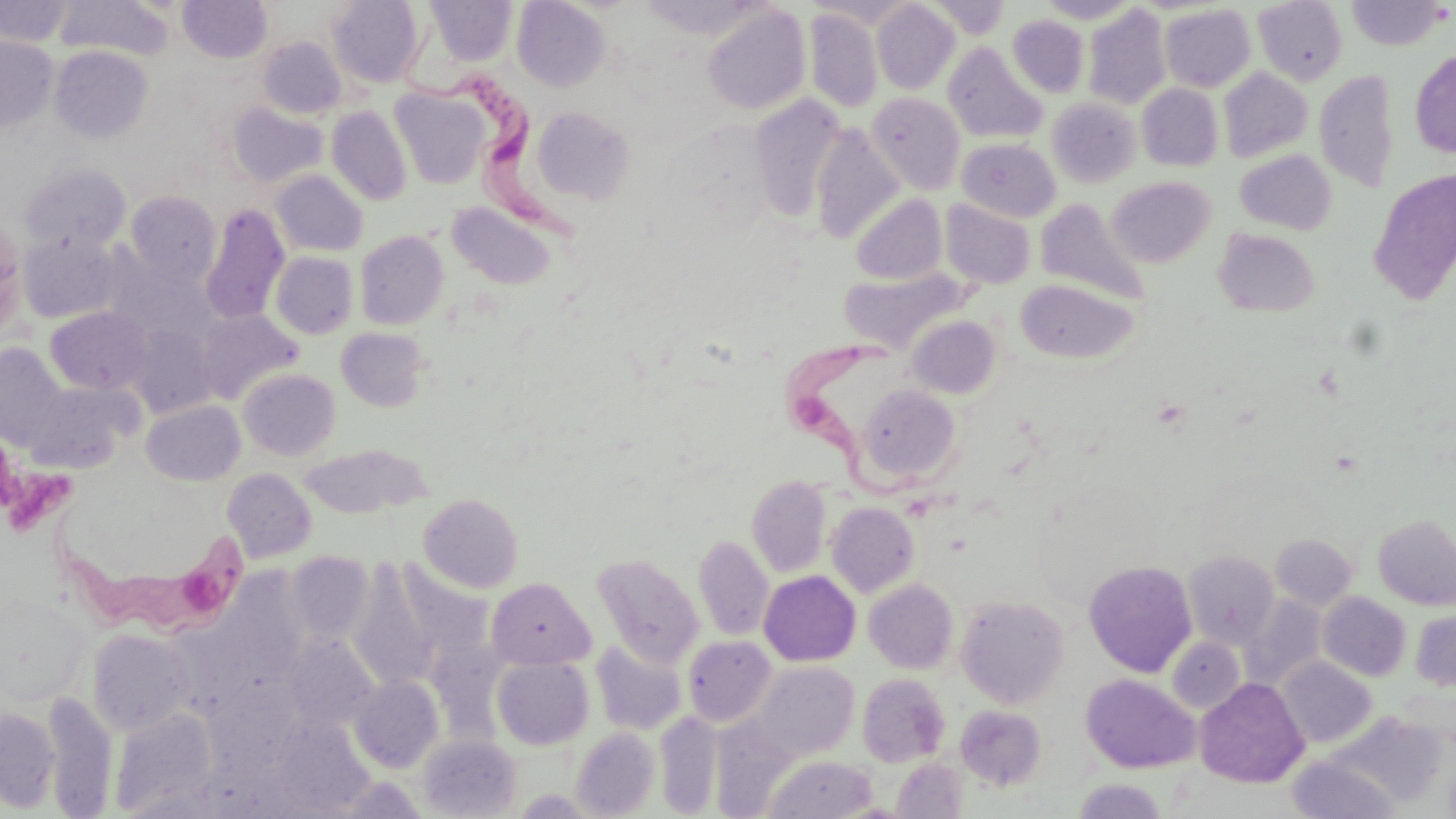
Summary:
  - Coordinate format: approximate bounding boxes as (x1,y1)-(x2,y2) corner pairs in pixels
  - Platelet locations: (11,475)-(72,536)
  - Uninfected red blood cell locations: (54,0)-(174,61), (327,0)-(425,88), (1036,0)-(1141,24), (1254,0)-(1348,85), (0,1)-(72,46), (178,1)-(272,62), (425,1)-(518,66), (512,1)-(610,91), (807,1)-(918,28), (925,1)-(1010,39), (1346,1)-(1449,50), (872,2)-(960,94), (1159,4)-(1256,92), (702,6)-(811,115), (1082,6)-(1171,109), (804,8)-(883,112), (1007,15)-(1090,97), (0,35)-(59,132), (258,36)-(346,119), (942,42)-(1047,144), (50,46)-(153,143), (1410,50)-(1456,158), (1218,68)-(1313,163), (1314,69)-(1399,193), (1137,83)-(1224,171), (391,87)-(490,189), (867,92)-(966,194), (749,94)-(847,222), (1047,97)-(1142,187), (228,102)-(328,187), (326,105)-(412,206), (533,105)-(636,203), (810,125)-(905,243), (957,137)-(1061,221), (1235,149)-(1336,234), (21,163)-(131,253), (1368,169)-(1456,303), (271,170)-(368,256), (1107,176)-(1215,267), (126,191)-(222,287), (850,193)-(947,284), (1035,198)-(1149,305), (940,199)-(1036,289), (446,201)-(557,290), (200,203)-(290,325), (0,219)-(26,334), (1214,228)-(1319,317), (355,230)-(449,330), (18,232)-(122,323), (271,252)-(358,339), (840,269)-(963,352), (1015,279)-(1140,364), (45,306)-(152,394), (196,309)-(303,404), (905,315)-(1002,399), (126,325)-(217,417), (335,327)-(431,411), (0,342)-(69,450), (238,369)-(341,460), (25,382)-(133,472), (856,384)-(961,487), (141,400)-(245,486), (300,443)-(429,518), (222,468)-(316,562), (747,474)-(831,577), (418,493)-(523,593), (826,501)-(920,597), (1373,514)-(1456,610), (1271,533)-(1358,610), (693,535)-(774,641), (1182,550)-(1280,649), (286,551)-(374,645), (592,553)-(704,668), (1084,560)-(1197,677), (349,564)-(445,690), (759,571)-(861,666), (486,577)-(594,670), (864,579)-(958,674), (1318,592)-(1411,681), (0,594)-(90,706), (956,595)-(1070,708), (1239,595)-(1326,690), (1410,610)-(1456,690), (87,629)-(194,735), (284,633)-(381,731), (683,635)-(776,727), (1167,637)-(1245,714), (591,639)-(687,735), (491,657)-(594,750), (1278,658)-(1377,748), (753,662)-(860,760), (857,673)-(951,767), (1081,674)-(1199,773), (349,675)-(443,772), (1195,678)-(1309,788), (41,692)-(118,816), (955,705)-(1047,791), (0,707)-(61,812), (110,707)-(218,815), (655,710)-(723,816), (1332,711)-(1449,807), (270,716)-(374,815), (572,728)-(660,817), (417,734)-(522,818), (764,753)-(879,819), (1287,755)-(1400,818), (891,758)-(968,818), (1074,778)-(1167,818)
  - Trypanosoma brucei locations: (402,35)-(575,247), (775,324)-(959,501), (44,505)-(251,639)
  - Slide-level diagnosis: Trypanosoma brucei
  - Magnification: 1000x
  - Modality: optical microscopy
  - Field of view: one of a larger specimen
  - Preparation: thin blood film
  - Image size: 1456×819 pixels
  - Stain: May-Grünwald-Giemsa